Locate every uninfected red blood cell.
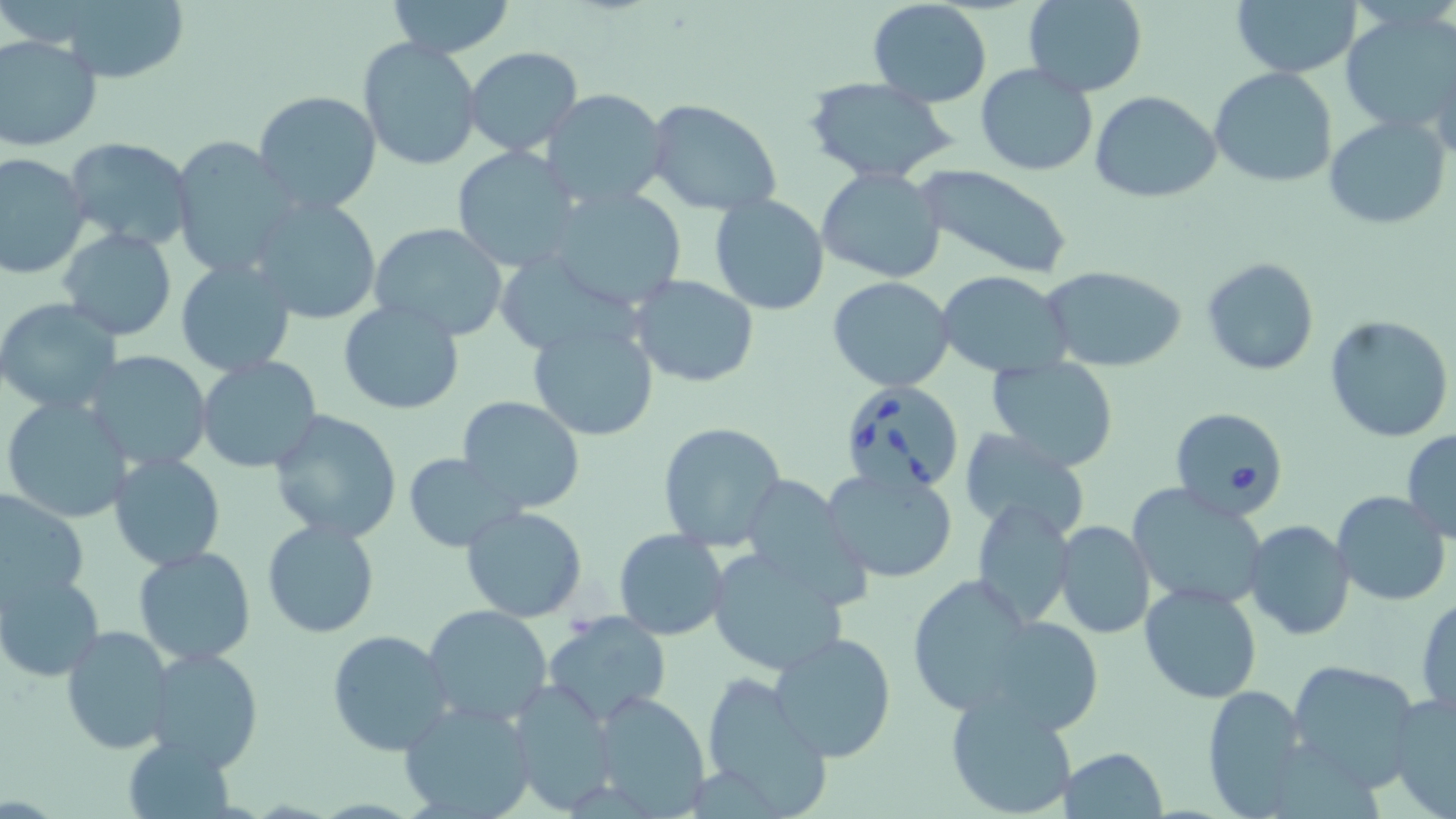

Approximate bounding boxes as (x1,y1)-(x2,y2) corner pairs in pixels.
Uninfected red blood cells: (384,0)-(516,57), (1231,0)-(1361,79), (34,1)-(196,84), (868,1)-(994,106), (1021,1)-(1148,97), (1340,9)-(1456,135), (0,34)-(103,152), (357,38)-(484,172), (464,46)-(583,155), (975,63)-(1098,175), (1211,68)-(1336,188), (804,76)-(959,186), (540,89)-(671,211), (251,90)-(383,216), (1090,90)-(1222,204), (647,100)-(781,219), (1325,116)-(1451,228), (63,137)-(197,252), (169,137)-(301,278), (450,146)-(585,271), (0,152)-(92,280), (917,165)-(1074,279), (816,167)-(948,282), (545,188)-(688,311), (249,194)-(382,326), (708,194)-(831,315), (369,221)-(511,340), (58,228)-(179,342), (496,252)-(660,355), (1201,255)-(1319,378), (175,257)-(297,379), (1040,264)-(1189,374), (939,271)-(1072,378), (630,274)-(760,388), (827,275)-(957,391), (0,298)-(123,417), (338,299)-(465,415), (1324,315)-(1454,444), (526,319)-(660,443), (83,349)-(213,472), (196,355)-(324,473), (984,357)-(1120,473), (2,395)-(133,524), (457,395)-(586,514), (267,410)-(403,544), (657,422)-(787,553), (956,429)-(1094,544), (1401,431)-(1456,541), (108,452)-(228,571), (404,453)-(523,551), (823,466)-(961,584), (738,473)-(869,604), (1126,483)-(1270,610), (0,485)-(89,612), (1332,490)-(1451,606), (971,499)-(1075,628), (461,505)-(586,623), (261,518)-(381,639), (1243,520)-(1355,641), (1054,522)-(1155,638), (613,530)-(729,641), (132,546)-(258,665), (705,547)-(852,676), (2,571)-(104,682), (905,575)-(1036,713), (1138,581)-(1262,704), (1415,595)-(1456,715), (423,604)-(553,726), (544,613)-(671,725), (979,613)-(1107,737), (61,624)-(173,754), (326,630)-(454,756), (769,631)-(897,762), (144,647)-(266,773), (1287,658)-(1425,788), (699,675)-(834,816), (504,684)-(616,813), (1201,685)-(1308,815), (587,690)-(710,815), (943,691)-(1079,819), (1387,692)-(1455,819), (397,699)-(539,819), (121,735)-(238,817), (1058,747)-(1169,819).

Babesia divergens-infected red blood cell locations: (837,379)-(966,498), (1168,406)-(1290,519). Slide-level diagnosis: Babesia divergens. May-Grünwald-Giemsa stain. Thin blood smear. 1000x magnification. Optical microscopy. Image is 1456×819 pixels. Single field of view.